Classify this cell by malaria status.
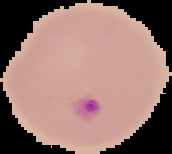

Parasitized.

image type = segmented cell region with the area outside set to black
image size = 172×154 pixels
preparation = thin blood smear